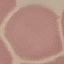
malaria status = uninfected
image type = cell patch, automatically extracted from a larger field of view and resized to 64 × 64 pixels
stain = Giemsa
preparation = thin blood film
capture = smartphone camera at the microscope eyepiece